Comment on the morphology of the red blood cells.
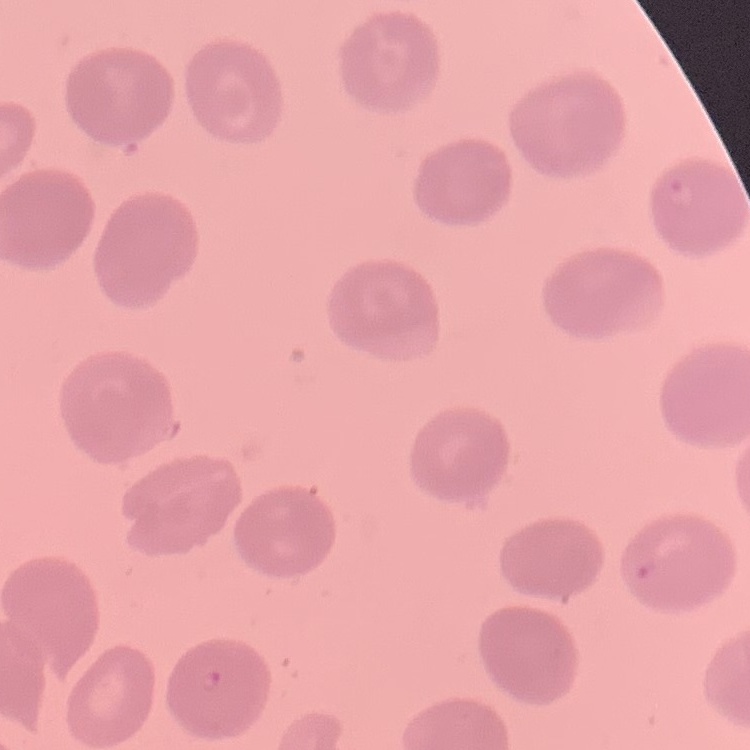
No rouleaux formation.

Summary:
  - Image type: square crop of a larger photomicrograph
  - Preparation: thin peripheral smear
  - Stain: Field's or Giemsa